Give the position of every Plasmodium parasite.
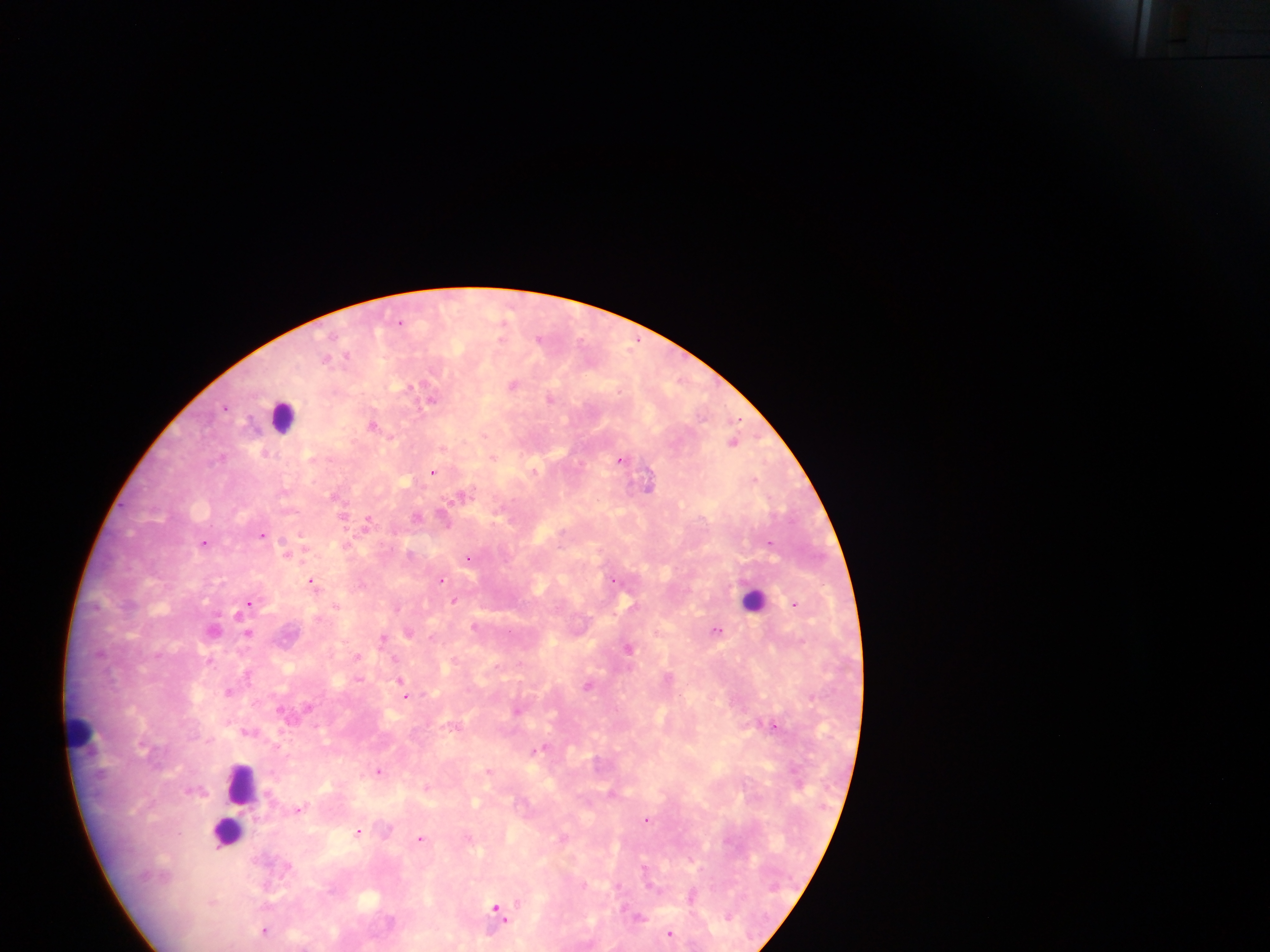
Approximate centers as x y in pixels.
Plasmodium parasites: 401 322; 540 337; 347 356; 514 384; 432 397; 551 398; 374 424; 734 442; 494 457; 622 459; 434 471; 649 483; 464 494; 343 516; 418 516; 445 518; 369 520; 264 534; 205 542; 770 542; 289 552; 469 557; 441 580; 615 580; 314 582; 455 600; 249 602; 796 604; 337 606; 398 607; 476 626; 213 629; 717 629; 249 632; 409 632; 384 637; 630 647; 210 660; 248 673; 670 678; 360 679; 401 679; 401 684; 590 684; 229 690; 812 695; 407 696; 518 710; 775 725; 250 731; 542 747; 379 770; 489 770; 427 786; 612 793; 300 809; 648 819; 360 831; 421 839; 692 895; 499 910; 639 916; 266 931; 671 932.

Leukocyte locations: 282 416; 754 599; 82 734; 242 784; 237 809; 228 833. Collected in Ghana. Photographed through a microscope with a mobile-phone camera. Image is 1270×952 pixels. Thick blood film. One field of view.